Assess this cell for malaria.
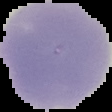
Uninfected.

image_type: segmented cell region with the area outside set to black
image_size: 112×112 pixels
preparation: thin blood film